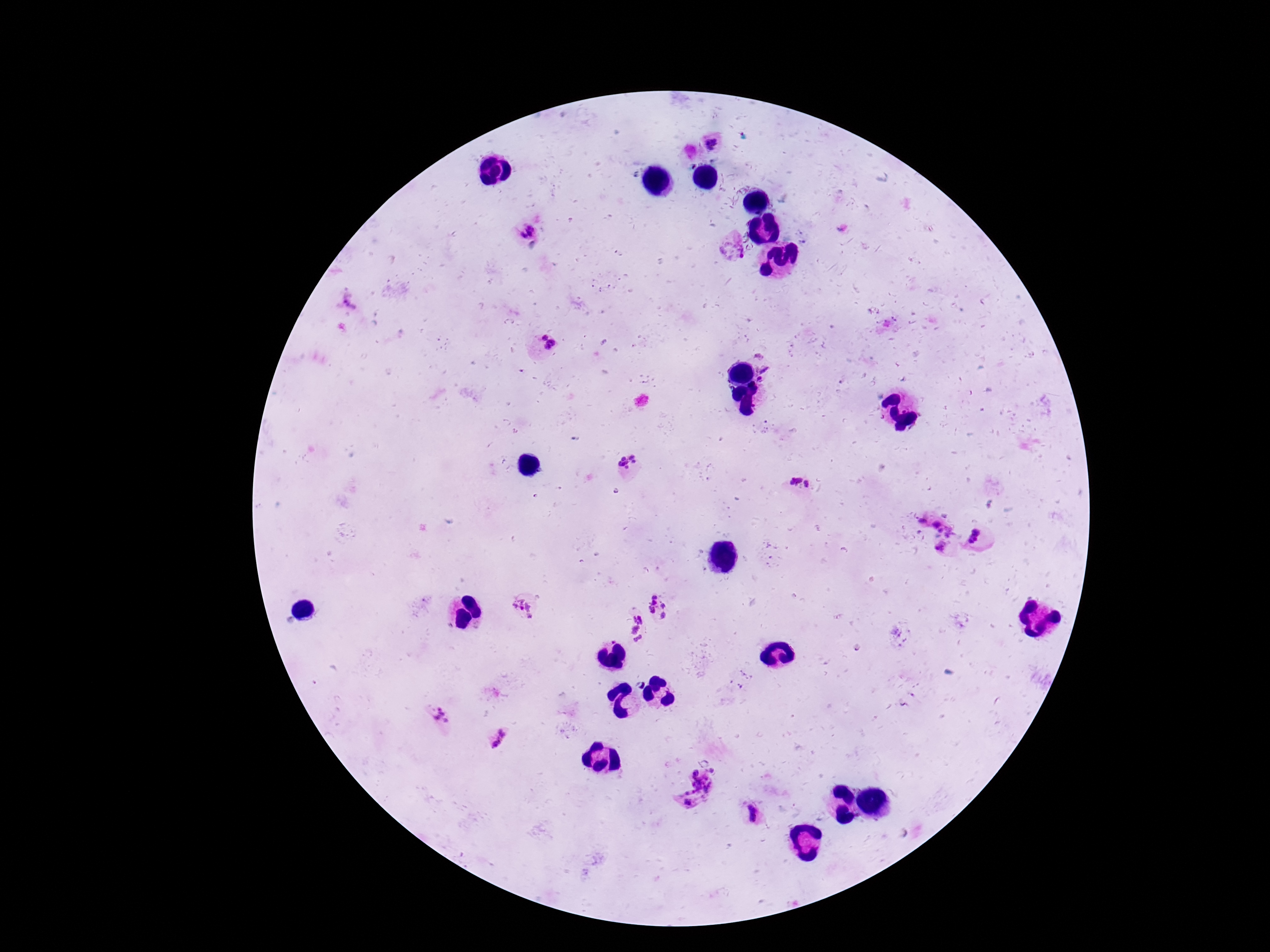 Approximate centers as [x, y] in pixels. Plasmodium parasite locations: [714, 143], [527, 231], [731, 246], [350, 303], [548, 341], [761, 356], [764, 370], [760, 381], [630, 464], [795, 480], [809, 485], [924, 518], [937, 523], [948, 530], [979, 536], [942, 545], [658, 604], [522, 610], [636, 627], [440, 715], [499, 738], [714, 770], [694, 773], [703, 784], [689, 798], [752, 812]. Image is 1270×952 pixels. Photographed through the microscope eyepiece with a smartphone camera. Thick blood film. 100x magnification. Single field of view. Giemsa stain. Patient malaria status: positive.